Point out each Plasmodium parasite.
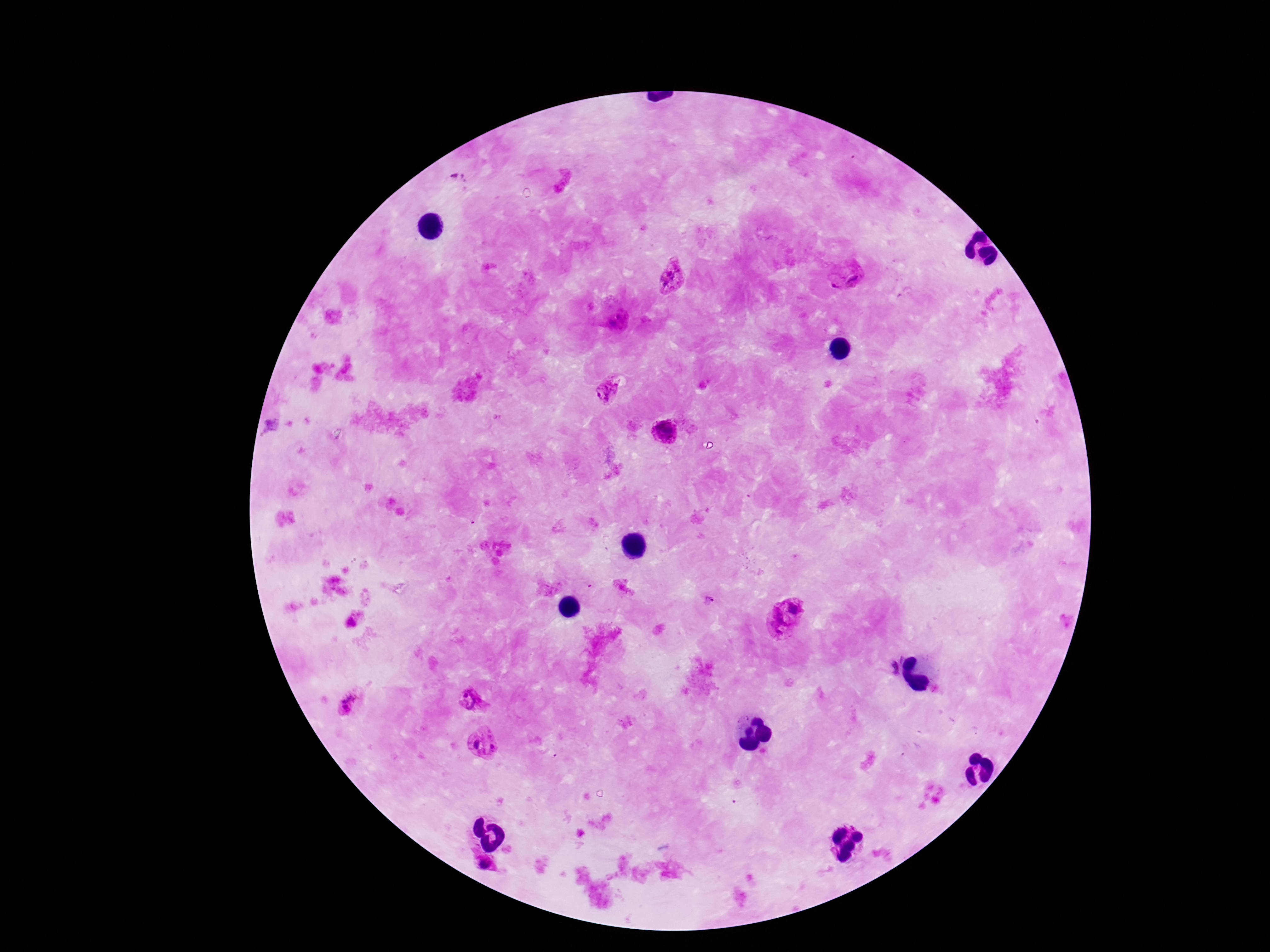

Approximate object centers, in pixels from the top-left corner.
Plasmodium parasites: (x=847, y=274), (x=672, y=275), (x=604, y=390), (x=664, y=433), (x=794, y=605), (x=776, y=623), (x=886, y=667), (x=472, y=699), (x=349, y=705), (x=483, y=740), (x=486, y=862).

Giemsa-stained preparation. Patient malaria status: positive. One field from this slide. Image is 1270×952 pixels. Photographed through the microscope eyepiece with a smartphone camera. Thick peripheral-blood smear. 100x magnification.